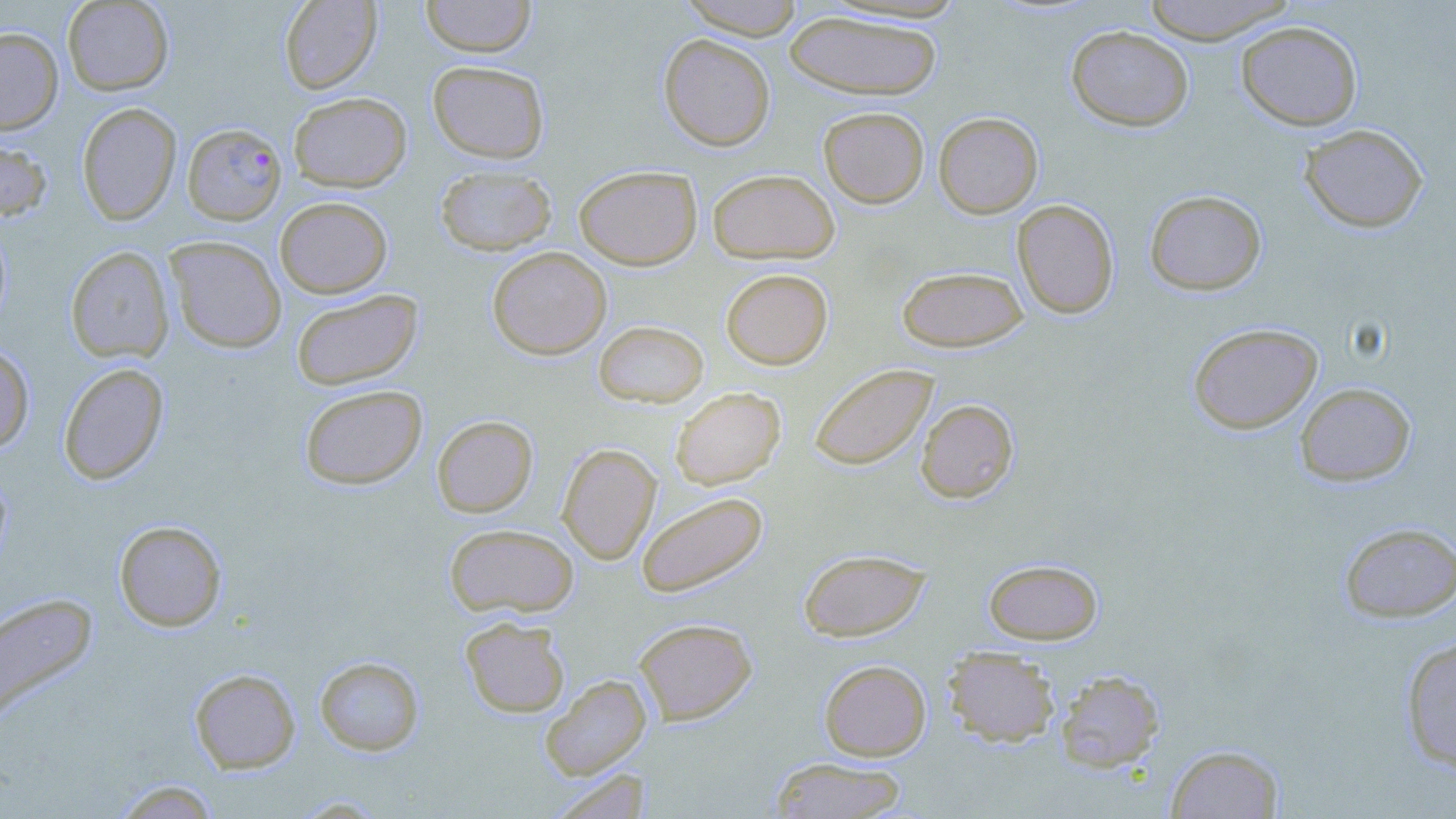

Summary:
  - Coordinate format: approximate bounding boxes as [x1, y1, x2, y2] in pixels
  - Uninfected red blood cell locations: [62, 0, 174, 95], [279, 0, 382, 94], [420, 0, 536, 58], [678, 0, 806, 39], [1139, 0, 1297, 44], [783, 10, 943, 100], [1236, 21, 1362, 130], [1066, 25, 1193, 132], [0, 27, 63, 134], [658, 34, 776, 151], [427, 60, 549, 164], [289, 92, 411, 192], [76, 102, 182, 225], [818, 106, 930, 208], [933, 112, 1043, 218], [1299, 123, 1428, 233], [0, 133, 53, 222], [434, 165, 557, 256], [574, 165, 702, 270], [707, 169, 840, 264], [1144, 189, 1267, 296], [274, 196, 393, 298], [1012, 199, 1119, 319], [0, 220, 13, 333], [165, 236, 287, 353], [65, 246, 174, 363], [487, 246, 612, 359], [896, 266, 1028, 352], [720, 268, 833, 369], [291, 289, 424, 390], [593, 320, 709, 408], [1188, 323, 1323, 434], [0, 344, 35, 454], [58, 362, 169, 485], [809, 363, 938, 471], [1295, 382, 1416, 486], [299, 384, 428, 490], [670, 387, 786, 489], [916, 399, 1019, 503], [432, 415, 538, 517], [557, 442, 661, 564], [0, 465, 12, 574], [636, 491, 768, 598], [114, 520, 227, 631], [1338, 521, 1456, 623], [444, 523, 579, 618], [798, 548, 931, 641], [983, 558, 1103, 645], [0, 592, 98, 728], [460, 617, 570, 718], [634, 617, 757, 724], [1399, 636, 1456, 773], [942, 646, 1060, 747], [314, 656, 425, 756], [819, 659, 931, 761], [190, 668, 301, 773], [1055, 670, 1165, 772], [541, 674, 652, 781], [1165, 744, 1285, 818], [769, 756, 909, 818], [547, 769, 652, 819], [110, 779, 223, 818]
  - Plasmodium falciparum-infected red blood cell locations: [182, 122, 287, 225]
  - Slide-level diagnosis: Plasmodium falciparum
  - Preparation: thin blood film
  - Stain: May-Grünwald-Giemsa
  - Field of view: one of a larger specimen
  - Modality: optical microscopy
  - Magnification: 1000x
  - Image size: 1456×819 pixels